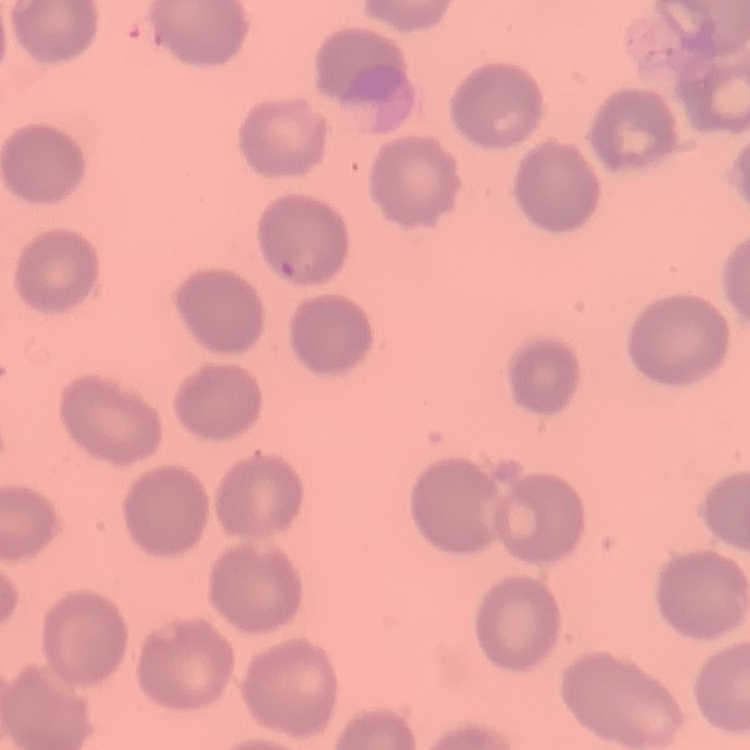

The erythrocytes exhibit no rouleaux formation. Thin blood smear. Stained with either Field's or Giemsa. Square crop of a larger photomicrograph.